Report the malaria status of this cell.
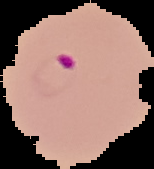

Parasitized.

{
  "preparation": "thin blood film",
  "image_type": "segmented cell region on a black background",
  "image_size": "154×169 pixels"
}